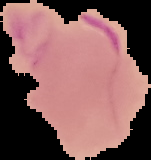 Malaria status: uninfected. Image is 151×160 pixels. From a thin blood smear. The area outside the segmented cell region is set to black.